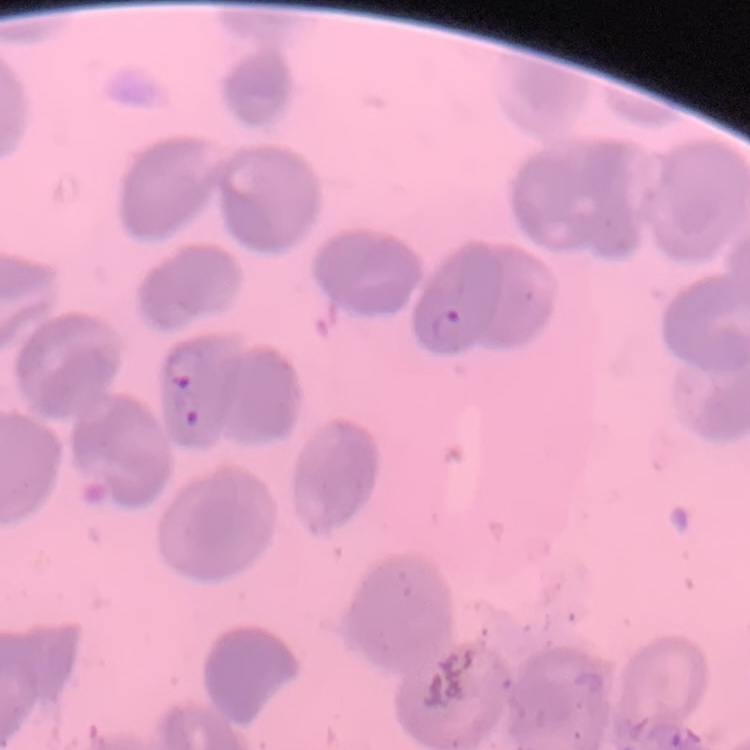

erythrocyte morphology = no rouleaux formation
stain = Field's or Giemsa
preparation = thin blood film
image type = square crop of a larger photomicrograph